Give the position of every malaria parasite.
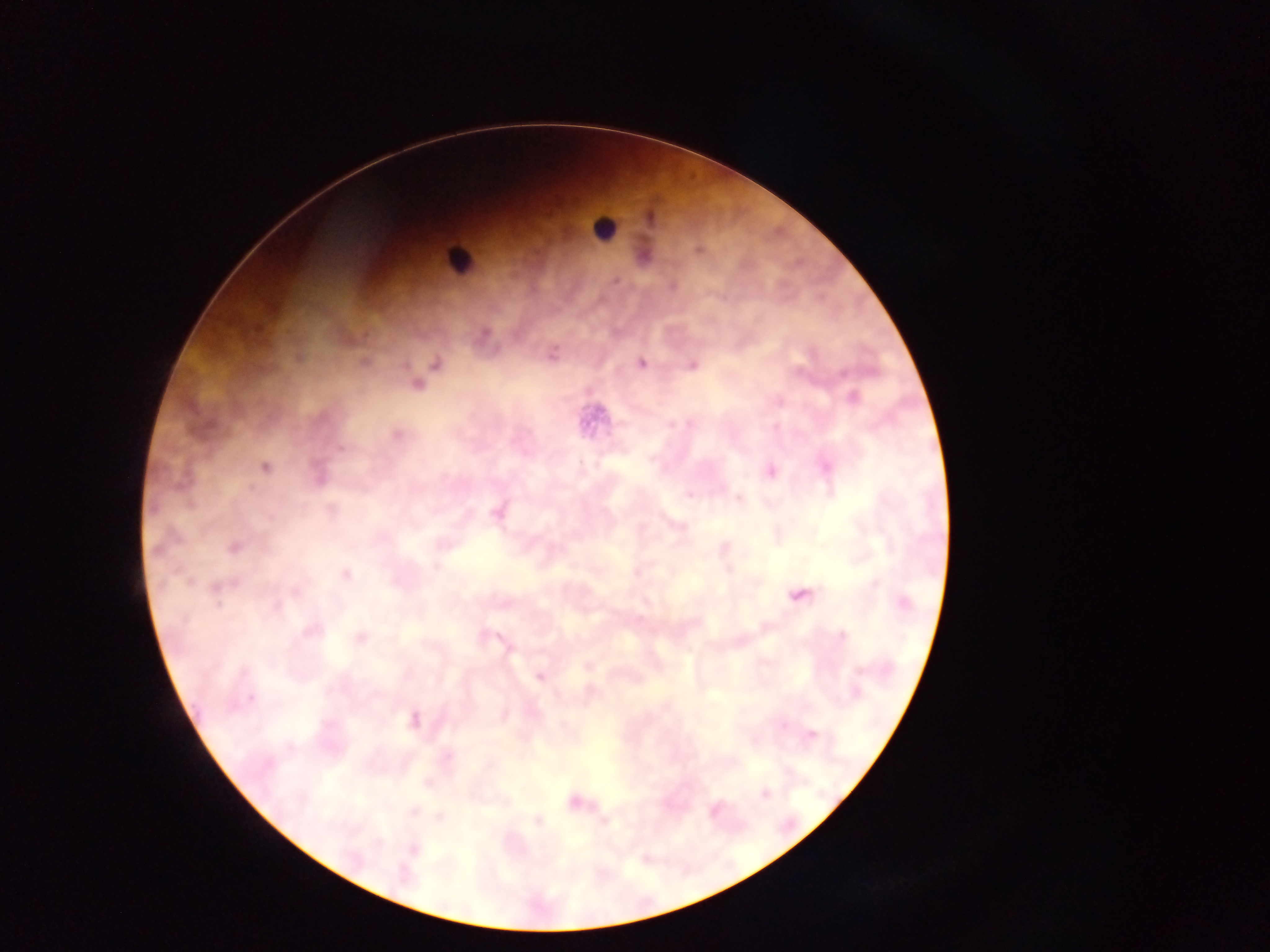
Approximate centers as (x, y) in pixels.
Malaria parasites: (698, 251), (616, 281), (672, 286), (485, 334), (552, 355), (364, 363), (640, 364), (436, 365), (692, 365), (842, 373), (418, 384), (853, 399), (397, 435), (341, 449), (265, 467), (771, 471), (318, 477), (689, 494), (739, 499), (331, 509), (496, 513), (234, 547), (728, 569), (637, 572), (346, 574), (218, 588), (800, 596), (277, 607), (311, 631), (490, 635), (842, 636), (360, 638), (589, 665), (540, 676), (591, 691), (251, 699), (413, 720), (783, 725), (812, 734), (765, 793), (573, 801), (414, 810), (440, 817), (538, 820), (414, 848).

field of view = single
leukocyte locations = approximate centers as (x, y) in pixels: (602, 228), (457, 260)
preparation = thick blood film
image size = 1270×952 pixels
capture = mobile-phone photograph through a microscope
country = Ghana